Report the malaria status of this cell.
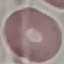

Uninfected.

{
  "preparation": "thin blood film",
  "stain": "Giemsa",
  "image_type": "cell patch, automatically extracted from a larger field of view and resized to 64 × 64 pixels",
  "capture": "smartphone through the microscope eyepiece"
}